Describe the morphology of the erythrocytes.
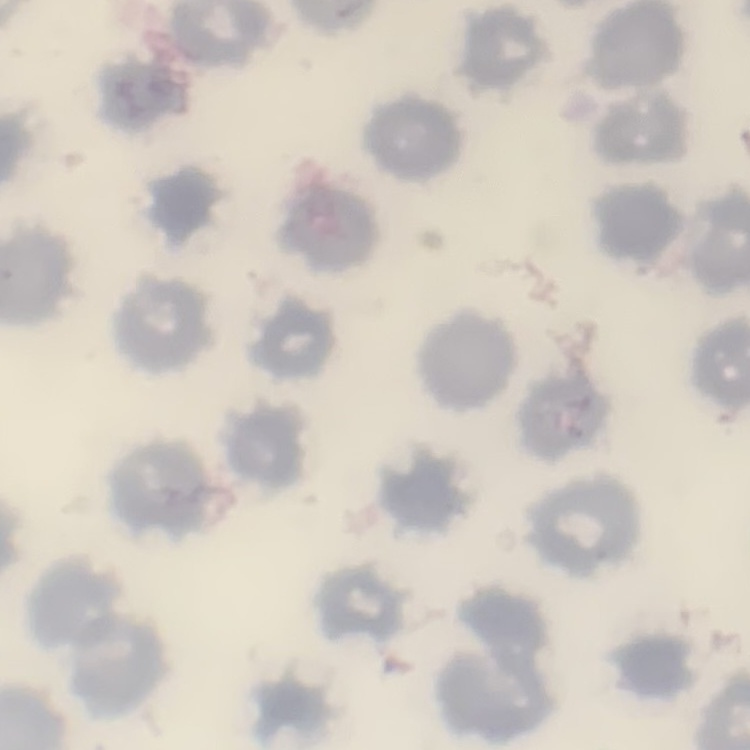

They show no rouleaux formation.

stain: Field's or Giemsa
preparation: thin blood film
image_type: square crop of a larger photomicrograph